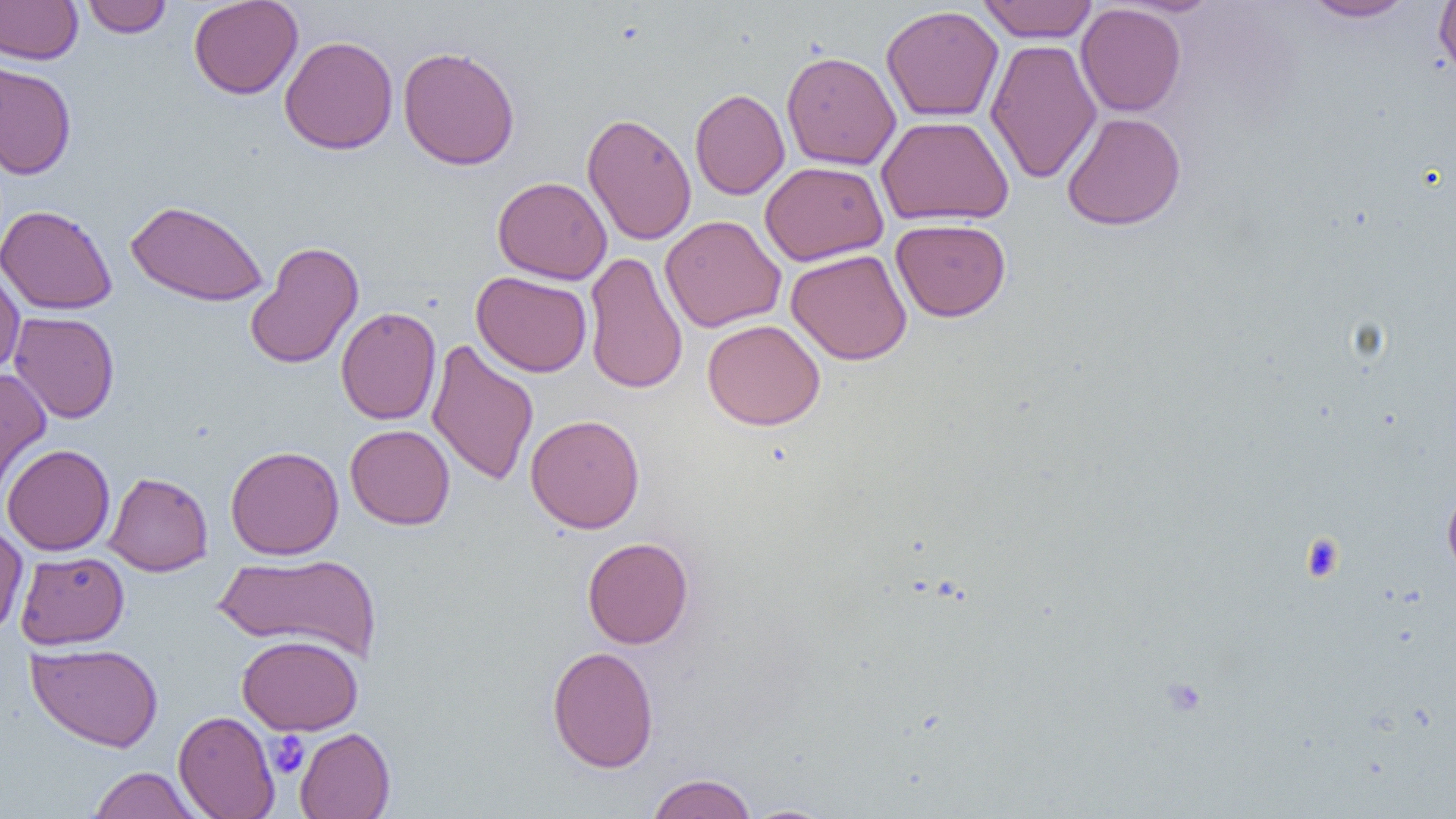
Approximate bounding boxes as [x1, y1, x2, y2] in pixels. Platelet locations: [1301, 534, 1345, 581], [268, 731, 309, 778]. Uninfected red blood cell locations: [81, 0, 172, 37], [188, 0, 303, 99], [978, 0, 1098, 43], [1298, 0, 1419, 23], [1434, 0, 1456, 81], [0, 1, 82, 65], [1076, 3, 1186, 117], [881, 5, 1004, 122], [280, 35, 398, 154], [985, 39, 1102, 184], [397, 45, 521, 171], [781, 50, 901, 170], [0, 62, 77, 179], [690, 88, 790, 200], [582, 112, 697, 246], [1061, 112, 1186, 231], [876, 115, 1014, 225], [759, 161, 889, 266], [492, 176, 612, 285], [125, 200, 269, 307], [0, 204, 117, 315], [660, 215, 786, 333], [891, 218, 1011, 321], [244, 240, 364, 370], [786, 249, 912, 365], [583, 251, 688, 395], [0, 264, 25, 379], [471, 271, 592, 377], [336, 306, 442, 425], [9, 311, 120, 423], [702, 319, 825, 430], [426, 339, 539, 487], [0, 367, 51, 500], [525, 413, 645, 534], [345, 424, 455, 530], [2, 444, 115, 555], [225, 445, 344, 559], [103, 471, 213, 576], [1442, 484, 1456, 580], [0, 521, 28, 638], [582, 536, 694, 649], [214, 550, 382, 663], [15, 551, 129, 650], [237, 634, 363, 734], [26, 642, 163, 752], [547, 645, 659, 773], [173, 710, 280, 819], [295, 727, 395, 819], [88, 766, 202, 818], [646, 773, 758, 819], [740, 804, 838, 819]. Slide-level diagnosis: negative for blood parasites. Thin blood smear. Image is 1456×819 pixels. Captured at 1000x magnification. Single field of view. Light microscopy.